Describe the morphology of the erythrocytes.
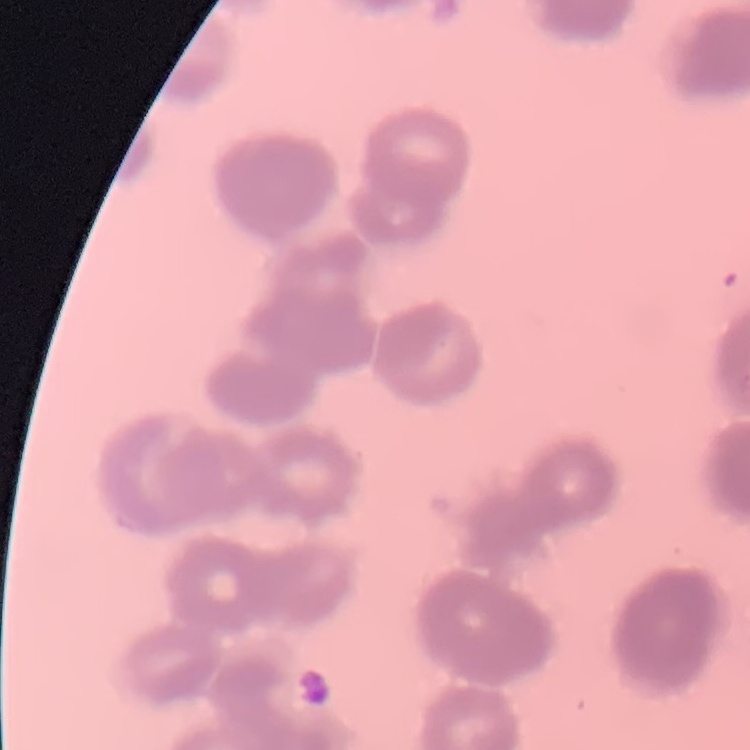
Rouleaux formation.

Summary:
  - Stain: Field's or Giemsa
  - Preparation: thin blood smear
  - Image type: one tile cut from a larger photomicrograph